Comment on the morphology of the red blood cells.
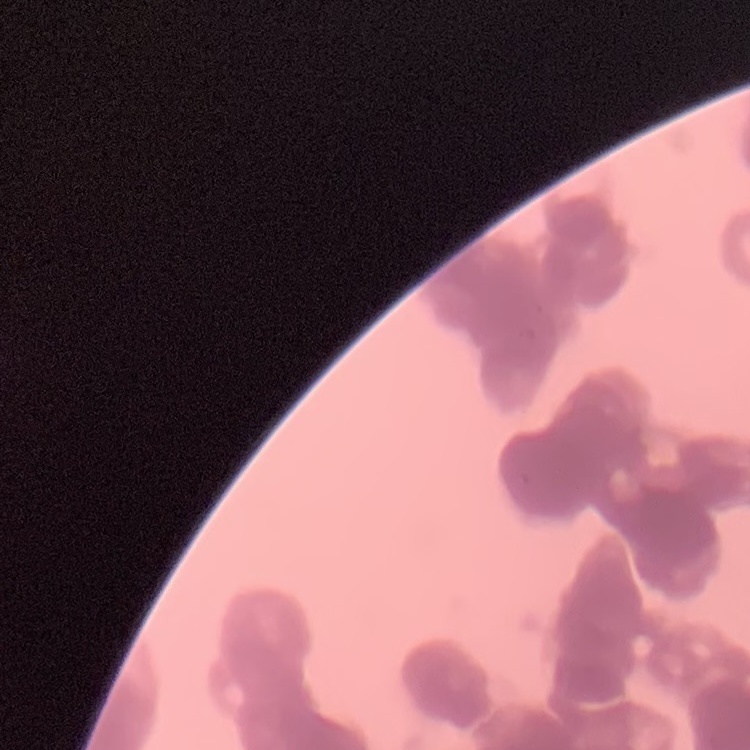

Rouleaux formation.

Summary:
  - Image type: square crop of a larger photomicrograph
  - Preparation: thin blood film
  - Stain: Field's or Giemsa